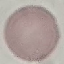

Summary:
  - Result: no malaria parasites seen
  - Capture: smartphone through the microscope eyepiece
  - Preparation: thin smear
  - Stain: Giemsa
  - Image type: automatically extracted cell patch, resized to 64 × 64 pixels